Report the malaria status of this cell.
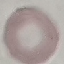
It is uninfected.

Summary:
  - Stain: Giemsa
  - Image type: automatically extracted cell patch, resized to 64 × 64 pixels
  - Preparation: thin smear
  - Capture: smartphone through the microscope eyepiece